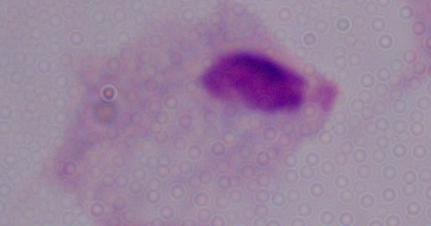

Summary:
  - Identification: trichomonad
  - Magnification: 1000x
  - Modality: photomicrograph